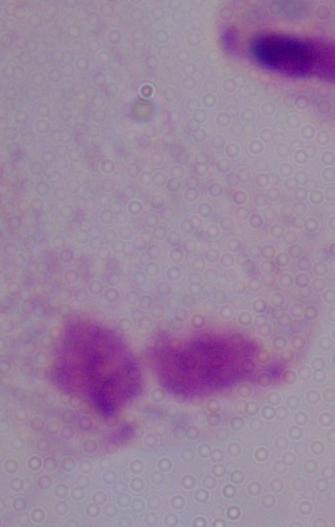

Summary:
  - Magnification: 1000x
  - Identification: trichomonad
  - Modality: micrograph